Give the position of every leukocyte visible.
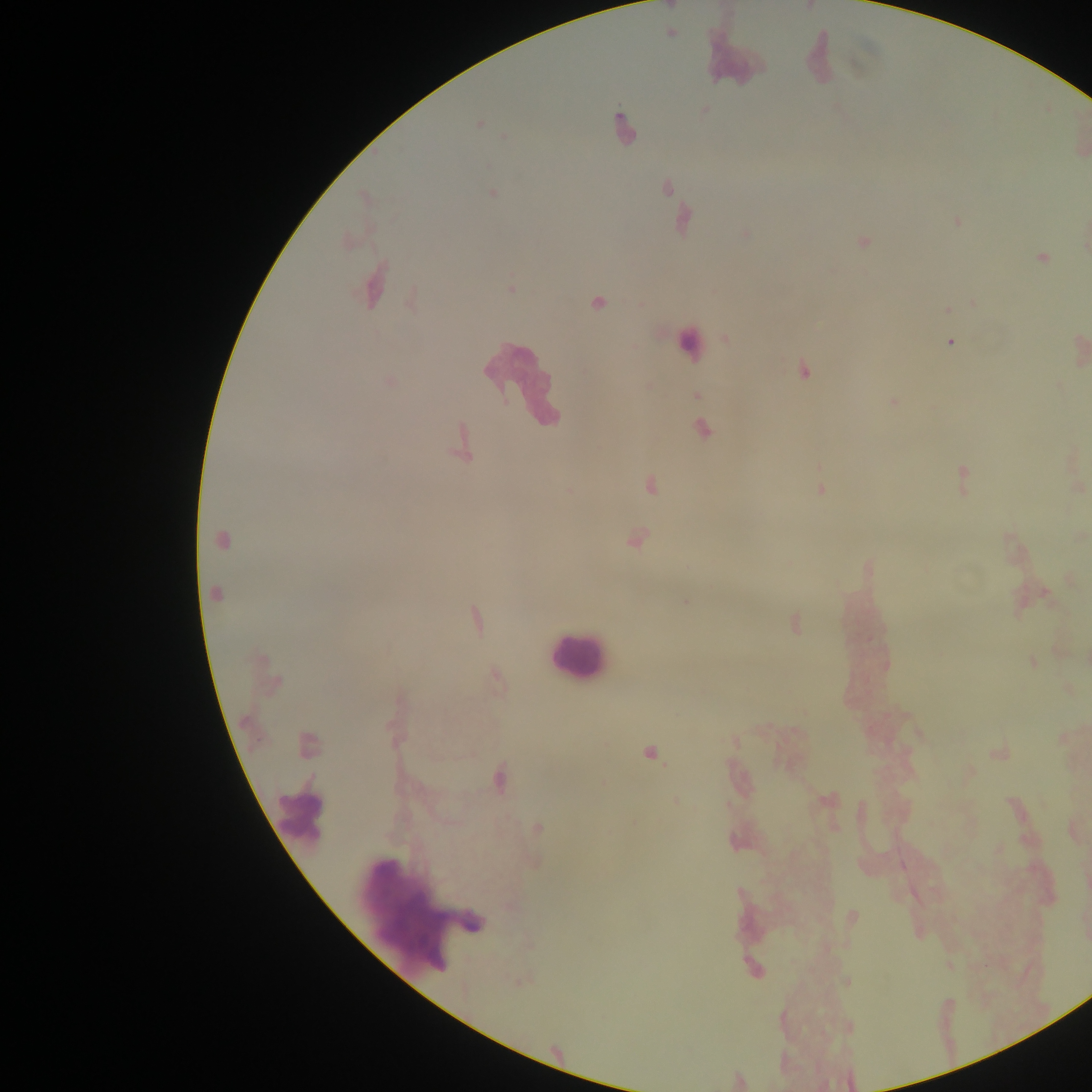
Approximate centers as [x, y] in pixels.
Leukocytes: [816, 59], [732, 60], [623, 128], [374, 285], [688, 347], [519, 385], [578, 658], [299, 815], [420, 908].

{
  "capture": "mobile-phone photograph through a microscope",
  "plasmodium_parasite_locations": "approximate centers as [x, y] in pixels: [669, 6], [809, 6], [670, 33], [478, 123], [665, 187], [492, 193], [675, 207], [682, 221], [957, 222], [745, 234], [862, 241], [1041, 257], [511, 288], [411, 297], [597, 302], [974, 304], [946, 309], [726, 338], [951, 342], [1079, 349], [802, 370], [389, 382], [697, 395], [893, 401], [701, 429], [462, 444], [961, 475], [649, 486], [820, 488], [569, 490], [635, 539], [222, 540], [868, 568], [1044, 593], [215, 595], [685, 600], [475, 621], [793, 623], [1033, 661], [268, 675], [496, 676], [394, 725], [1061, 738], [307, 745], [650, 753], [998, 753], [498, 777], [827, 799], [676, 800], [536, 829], [1073, 831], [851, 916], [753, 969], [739, 1081]",
  "preparation": "thick blood film",
  "country": "Ghana",
  "image_size": "1092×1092 pixels",
  "field_of_view": "single"
}